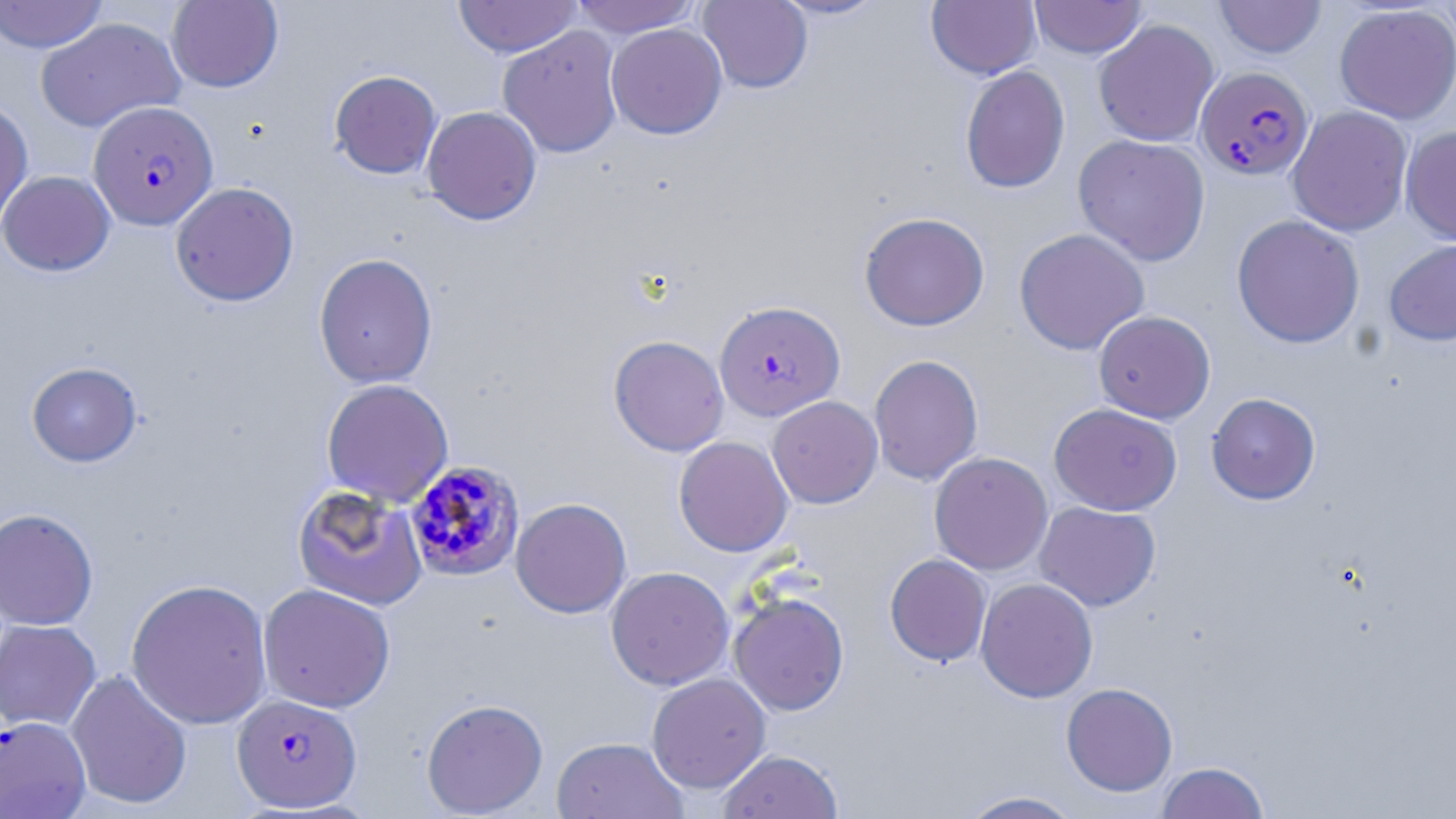
{
  "slide_level_diagnosis": "Plasmodium falciparum",
  "preparation": "thin blood smear",
  "magnification": "1000x",
  "uninfected_red_blood_cell_locations_subset": "approximate bounding boxes as named x1/y1/x2/y2 corners in pixels: (x1=0, y1=0, x2=109, y2=53), (x1=166, y1=0, x2=283, y2=92), (x1=453, y1=0, x2=581, y2=58), (x1=569, y1=0, x2=702, y2=37), (x1=771, y1=0, x2=888, y2=20), (x1=926, y1=0, x2=1041, y2=80), (x1=1029, y1=0, x2=1147, y2=59), (x1=1214, y1=0, x2=1326, y2=59), (x1=698, y1=1, x2=813, y2=94), (x1=1334, y1=3, x2=1456, y2=124), (x1=35, y1=17, x2=185, y2=132), (x1=1094, y1=19, x2=1219, y2=147), (x1=606, y1=23, x2=728, y2=139), (x1=498, y1=25, x2=624, y2=158), (x1=960, y1=65, x2=1070, y2=194), (x1=329, y1=70, x2=442, y2=179), (x1=0, y1=98, x2=33, y2=234), (x1=1287, y1=105, x2=1413, y2=236), (x1=421, y1=106, x2=542, y2=225), (x1=1400, y1=125, x2=1456, y2=246), (x1=1072, y1=134, x2=1211, y2=265), (x1=0, y1=170, x2=115, y2=276), (x1=169, y1=182, x2=299, y2=307), (x1=859, y1=212, x2=989, y2=331), (x1=1231, y1=214, x2=1365, y2=349), (x1=1014, y1=228, x2=1150, y2=355), (x1=1384, y1=238, x2=1456, y2=346), (x1=314, y1=253, x2=438, y2=389), (x1=1093, y1=310, x2=1215, y2=423), (x1=608, y1=335, x2=729, y2=456), (x1=868, y1=354, x2=983, y2=485), (x1=26, y1=362, x2=142, y2=467), (x1=321, y1=379, x2=454, y2=506), (x1=1206, y1=392, x2=1321, y2=504), (x1=767, y1=396, x2=883, y2=508), (x1=1049, y1=402, x2=1182, y2=515), (x1=674, y1=435, x2=794, y2=557), (x1=929, y1=452, x2=1053, y2=575), (x1=292, y1=485, x2=429, y2=611), (x1=511, y1=497, x2=632, y2=618), (x1=1034, y1=501, x2=1161, y2=611), (x1=0, y1=508, x2=99, y2=631), (x1=885, y1=553, x2=992, y2=666), (x1=606, y1=566, x2=734, y2=690), (x1=975, y1=577, x2=1098, y2=703), (x1=126, y1=579, x2=273, y2=729), (x1=257, y1=583, x2=396, y2=713), (x1=729, y1=592, x2=850, y2=716), (x1=0, y1=618, x2=101, y2=731), (x1=66, y1=669, x2=192, y2=810), (x1=647, y1=672, x2=771, y2=793), (x1=1061, y1=683, x2=1178, y2=797), (x1=421, y1=698, x2=548, y2=817), (x1=550, y1=736, x2=688, y2=819), (x1=717, y1=749, x2=844, y2=819), (x1=1156, y1=761, x2=1270, y2=819), (x1=955, y1=790, x2=1087, y2=818)",
  "field_of_view": "single",
  "stain": "May-Grünwald-Giemsa",
  "image_size": "1456×819 pixels",
  "plasmodium_falciparum_infected_red_blood_cell_locations_subset": "approximate bounding boxes as named x1/y1/x2/y2 corners in pixels: (x1=1195, y1=66, x2=1314, y2=180), (x1=88, y1=101, x2=218, y2=231), (x1=714, y1=300, x2=845, y2=422), (x1=405, y1=459, x2=525, y2=582), (x1=231, y1=693, x2=362, y2=813)",
  "modality": "optical microscopy"
}